Comment on the morphology of the red blood cells.
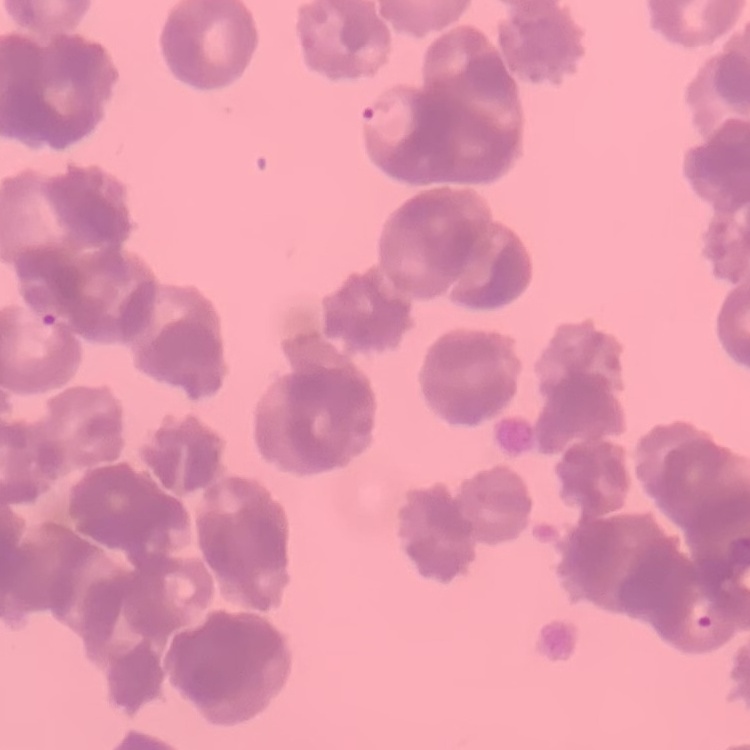

Rouleaux formation.

stain = Field's or Giemsa
preparation = thin blood smear
image type = one tile cut from a larger photomicrograph